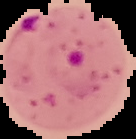

image size = 136×139 pixels
malaria status = parasitized
image type = segmented cell region with the area outside set to black
preparation = thin blood film